Give the position of every Plasmodium parasite visible.
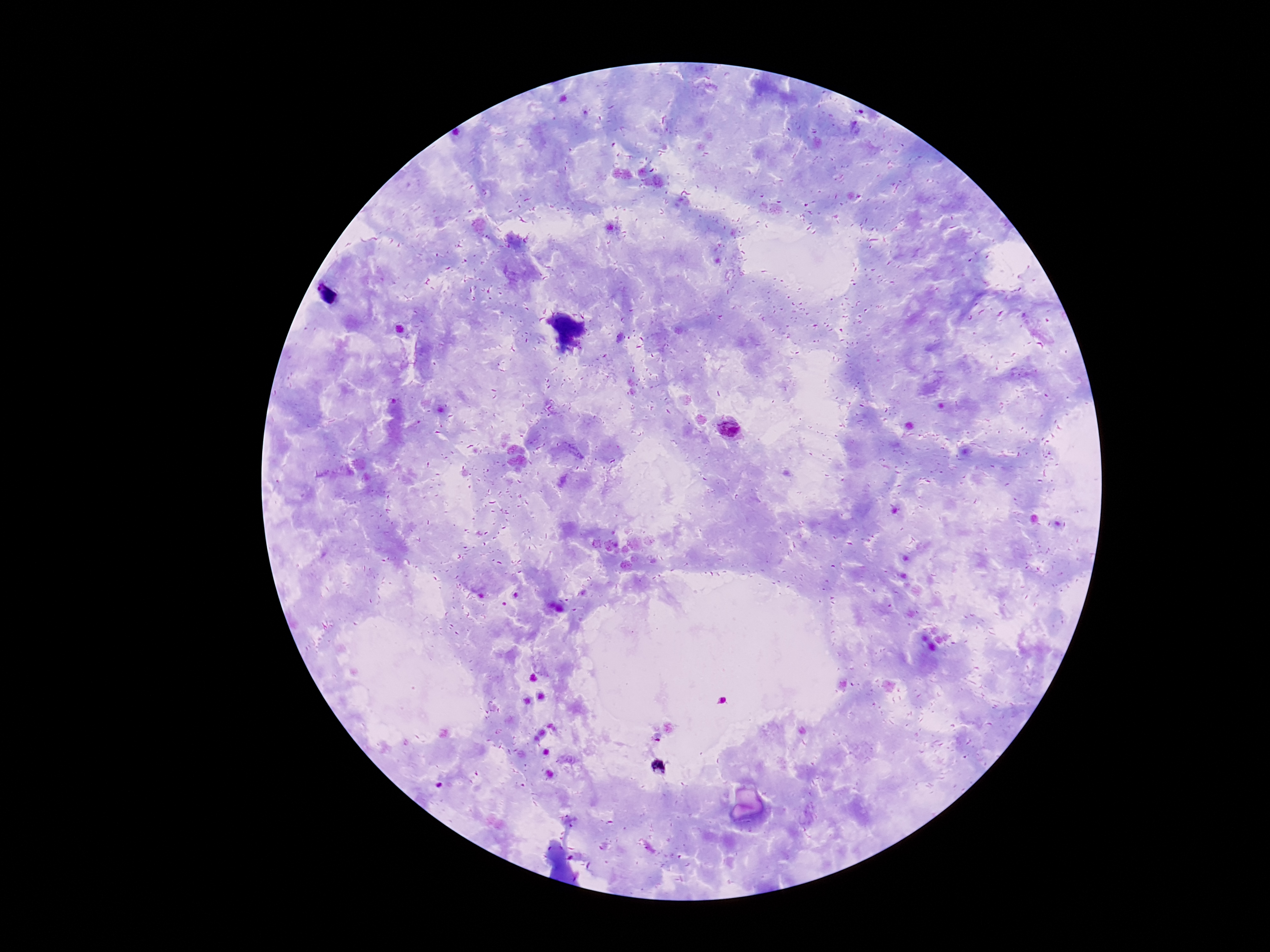

Approximate centers as {x, y} in pixels.
Plasmodium parasites: {726, 428}, {658, 767}.

{
  "preparation": "thick blood film",
  "magnification": "100x",
  "capture": "smartphone camera through the microscope eyepiece",
  "image_size": "1270×952 pixels",
  "patient_malaria_status": "infected",
  "stain": "Giemsa",
  "field_of_view": "single"
}